Assess the morphology of the erythrocytes.
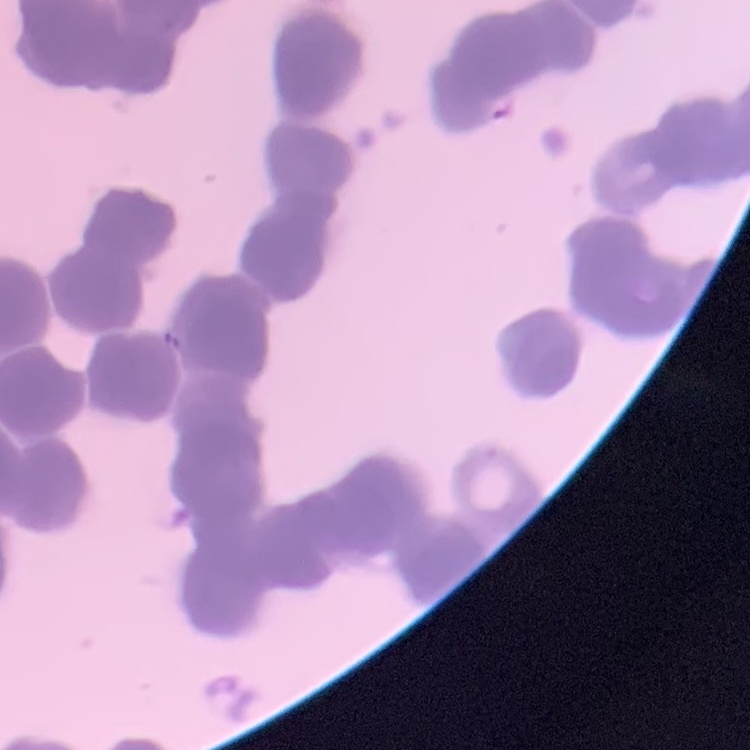

Rouleaux formation.

Field's or Giemsa stain. Thin blood smear. One tile cut from a larger photomicrograph.